Give the position of every Plasmodium parasite visible.
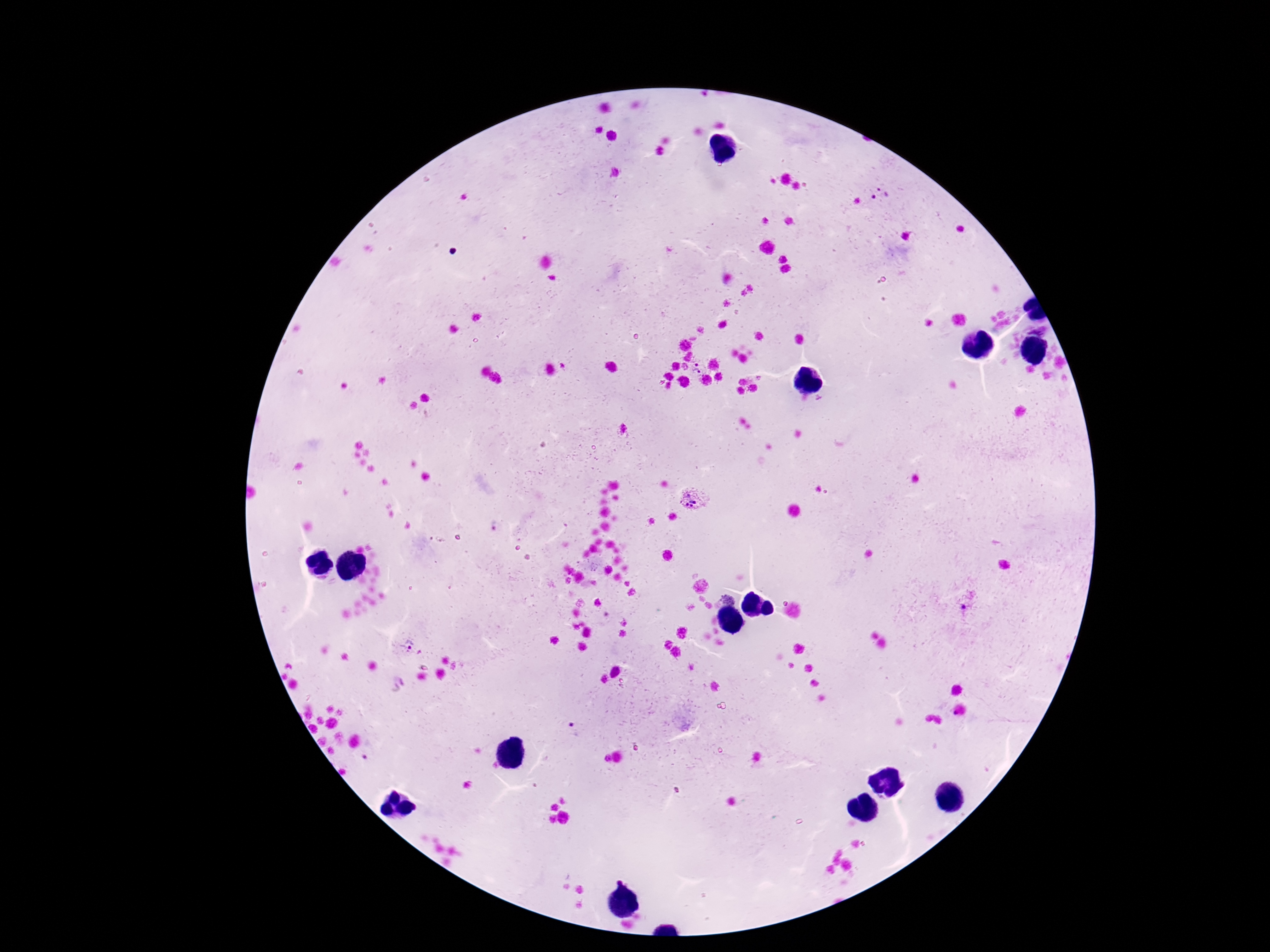

Approximate centers as [x, y] in pixels.
Plasmodium parasites: [881, 194], [1039, 331], [697, 368], [695, 498], [728, 595], [410, 645], [572, 728], [371, 754].

{
  "image_size": "1270×952 pixels",
  "capture": "smartphone camera through the microscope eyepiece",
  "preparation": "thick blood film",
  "patient_malaria_status": "positive",
  "magnification": "100x",
  "field_of_view": "single",
  "stain": "Giemsa"
}